Comment on the morphology of the red blood cells.
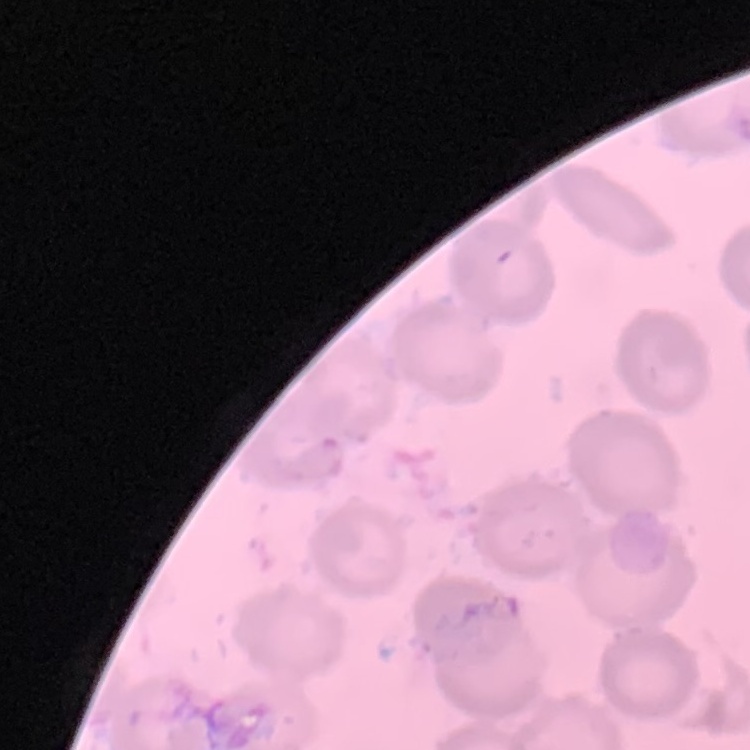

They show no rouleaux formation.

preparation = thin peripheral smear
image type = one tile cut from a larger photomicrograph
stain = Field's or Giemsa